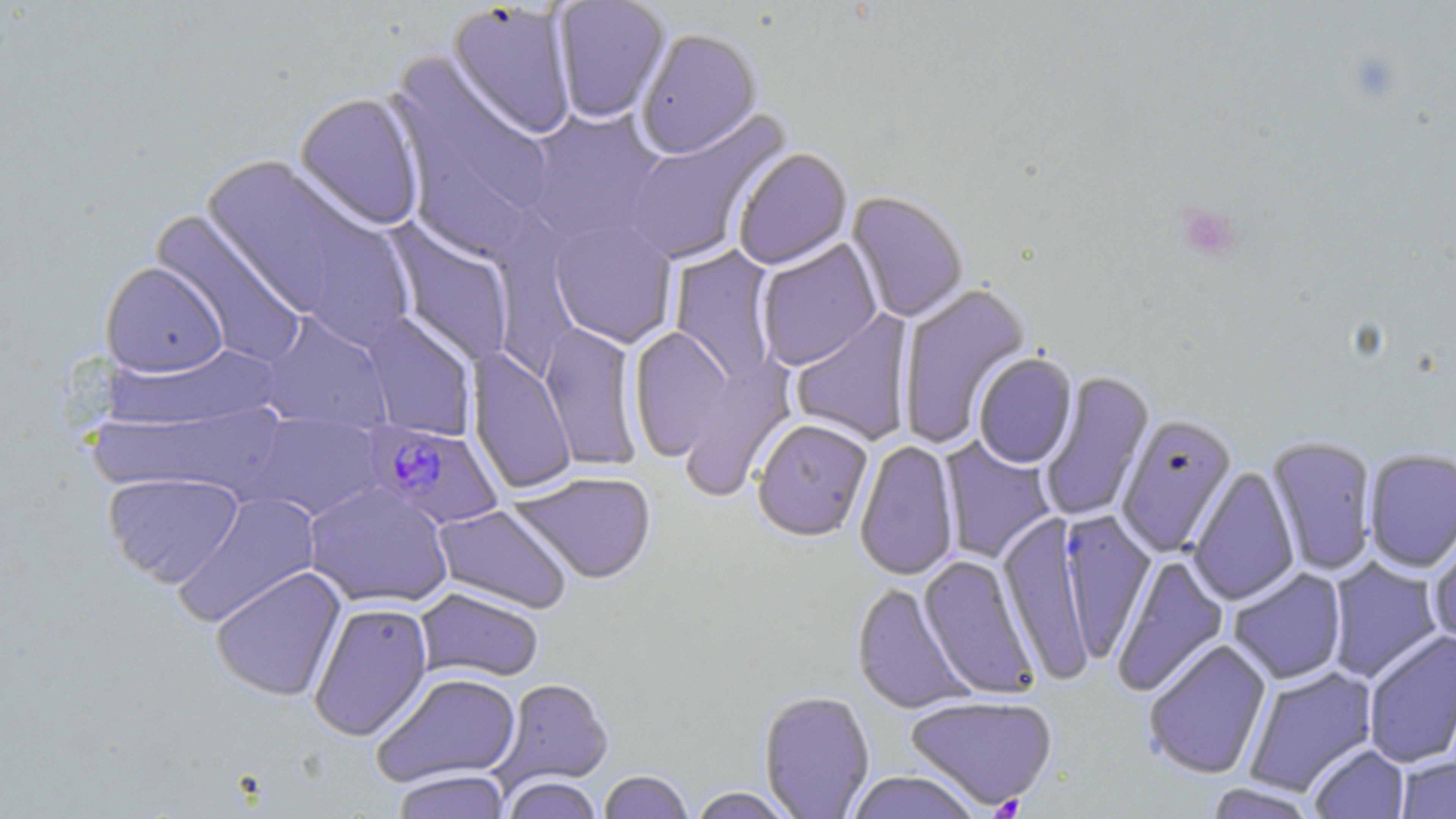

Summary:
  - Coordinate format: approximate bounding boxes as (x1, y1, x2, y2) in pixels
  - Platelet locations: (1175, 201, 1243, 263)
  - Plasmodium falciparum-infected red blood cell locations: (361, 421, 505, 531)
  - Uninfected red blood cell locations: (552, 1, 671, 125), (445, 2, 578, 142), (636, 30, 762, 161), (385, 53, 555, 244), (293, 92, 427, 232), (521, 107, 668, 249), (622, 108, 793, 267), (733, 149, 853, 271), (199, 155, 406, 333), (845, 192, 968, 323), (150, 209, 308, 367), (548, 217, 678, 349), (385, 221, 517, 368), (756, 239, 882, 371), (669, 246, 780, 387), (100, 261, 228, 377), (896, 283, 1032, 450), (790, 309, 915, 446), (255, 311, 394, 432), (359, 311, 477, 442), (539, 321, 643, 472), (629, 326, 736, 464), (671, 345, 800, 502), (466, 347, 577, 496), (973, 354, 1077, 469), (1038, 370, 1155, 523), (241, 412, 386, 522), (1117, 414, 1237, 557), (752, 420, 873, 544), (1265, 435, 1378, 576), (938, 436, 1057, 564), (854, 441, 960, 581), (1363, 447, 1456, 573), (1188, 466, 1300, 606), (508, 471, 657, 586), (103, 472, 245, 587), (303, 482, 454, 609), (171, 491, 322, 627), (432, 504, 573, 614), (1056, 509, 1156, 664), (998, 511, 1097, 688), (1427, 523, 1456, 650), (1111, 553, 1230, 699), (917, 555, 1041, 700), (1326, 557, 1444, 683), (210, 566, 347, 702), (1227, 568, 1348, 685), (851, 583, 975, 715), (414, 588, 544, 683), (308, 601, 433, 741), (1363, 630, 1456, 769), (1142, 639, 1272, 781), (1243, 667, 1378, 797), (370, 671, 522, 788), (492, 677, 614, 794), (758, 691, 875, 819), (904, 695, 1059, 812), (1308, 744, 1409, 819), (1396, 756, 1456, 819), (391, 769, 512, 819), (598, 770, 693, 819), (845, 771, 982, 819), (501, 777, 603, 819), (1203, 783, 1322, 819), (688, 787, 798, 818)
  - Slide-level diagnosis: Plasmodium falciparum
  - Image size: 1456×819 pixels
  - Modality: light microscopy
  - Stain: May-Grünwald-Giemsa
  - Preparation: thin blood film
  - Magnification: 1000x
  - Field of view: single